Name the parasite shown.
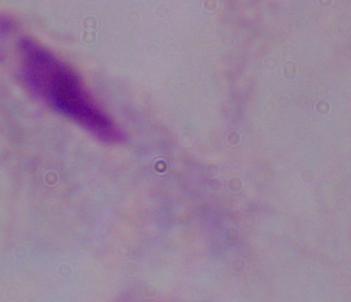
A trichomonad.

Micrograph. 1000x magnification.